Assess the morphology of the red blood cells.
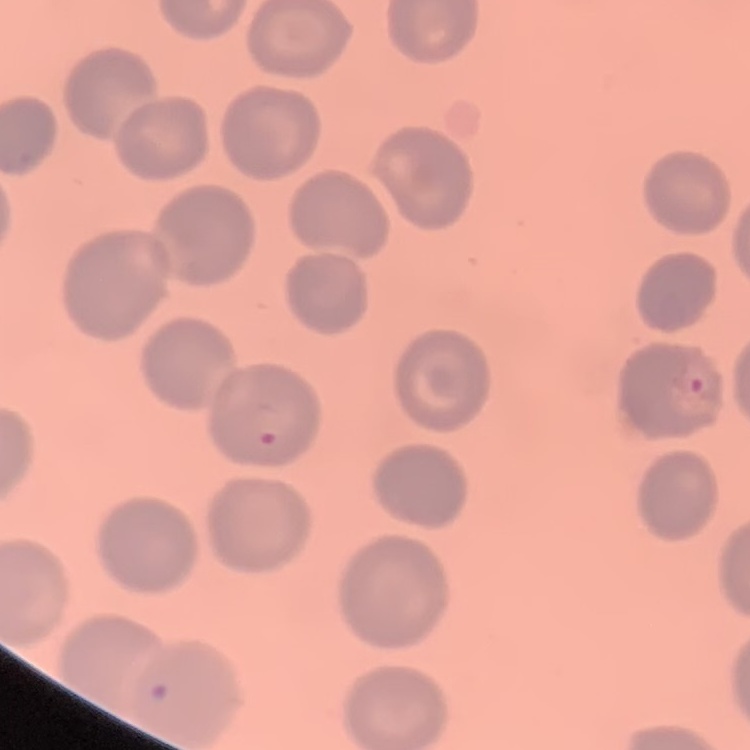
No rouleaux formation.

Thin blood film. Square crop of a larger photomicrograph. Field's or Giemsa stain.